Classify this cell by malaria status.
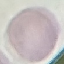

It is uninfected.

Thin blood film. Giemsa stain. Photographed with a smartphone camera at the microscope eyepiece. Cell patch, automatically extracted from a larger field of view and resized to 64 × 64 pixels.